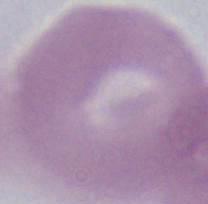

Summary:
  - Identification: red blood cell
  - Magnification: 1000x
  - Modality: photomicrograph